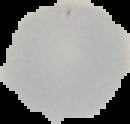
result = negative for Plasmodium parasites
preparation = thin blood smear
image size = 130×124 pixels
image type = segmented cell region with the area outside set to black